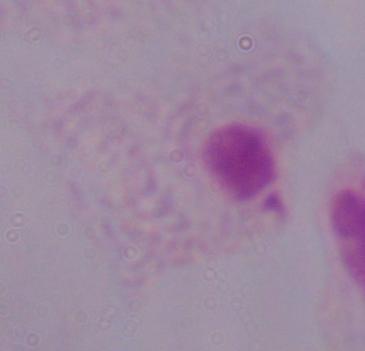 Captured at 1000x magnification. A trichomonad is seen. Photomicrograph.